Report the malaria status of this cell.
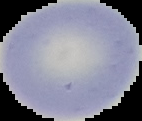

Uninfected.

Summary:
  - Image type: cell region segmented out of the field of view; surrounding area masked to black
  - Image size: 142×121 pixels
  - Preparation: thin blood smear